Classify this cell by malaria status.
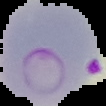

It is parasitized.

From a thin blood smear. Cell region segmented out of the field of view; the surrounding area is masked to black. Image is 106×106 pixels.